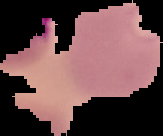

Summary:
  - Image size: 163×136 pixels
  - Malaria status: parasitized
  - Image type: segmented cell region on a black background
  - Preparation: thin blood smear